Locate every blood parasite and identify its species.
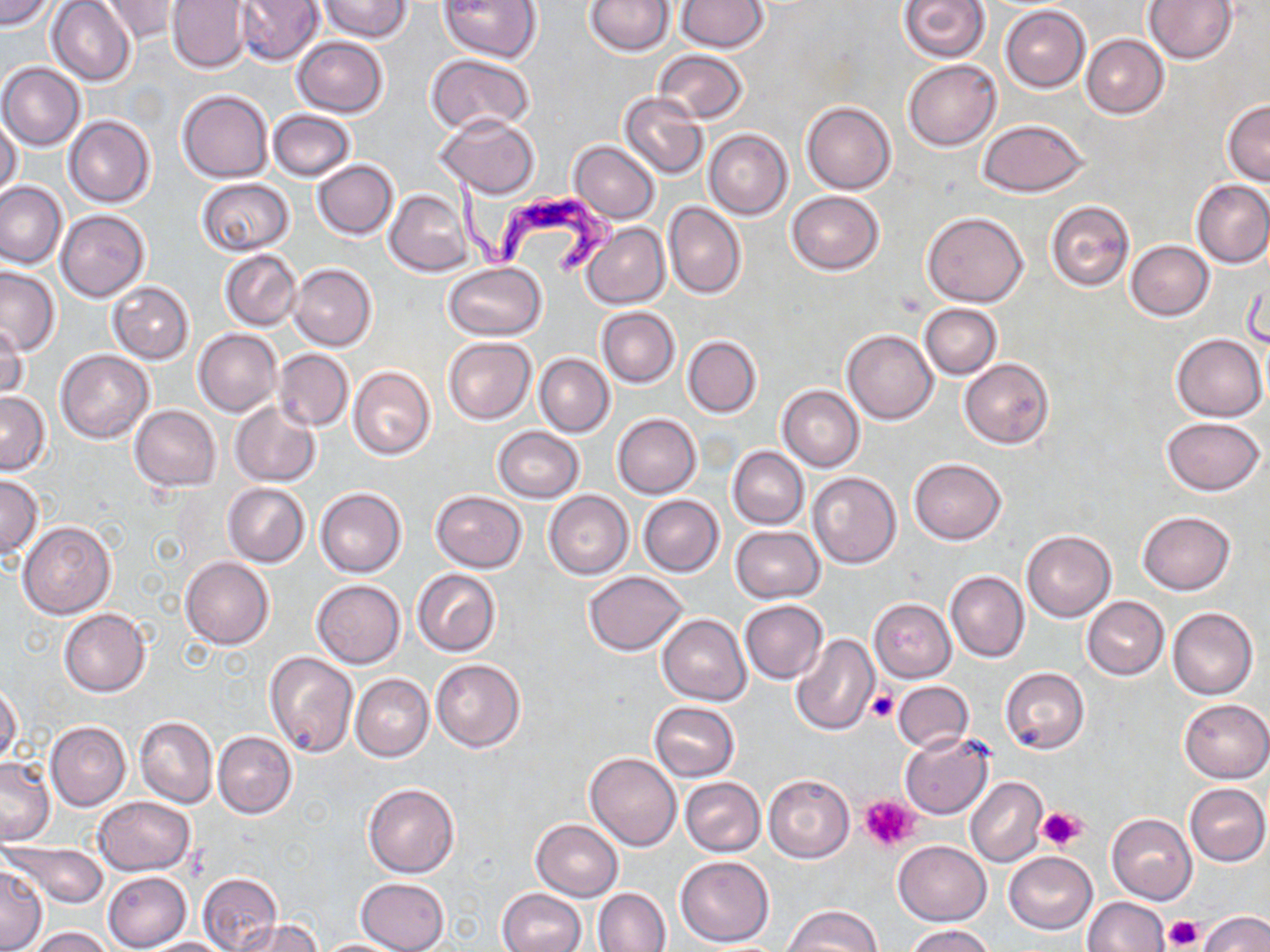
Approximate bounding boxes as [x1, y1, x2, y2] in pixels.
Trypanosoma brucei: [450, 177, 622, 278].
No Plasmodium falciparum, Plasmodium ovale, Plasmodium malariae, Plasmodium vivax, or Babesia divergens observed.

Uninfected red blood cell locations: [0, 0, 54, 31], [100, 0, 181, 43], [167, 0, 252, 73], [233, 0, 324, 66], [317, 0, 412, 41], [437, 0, 543, 63], [676, 0, 768, 52], [897, 0, 990, 62], [1144, 0, 1238, 64], [47, 1, 136, 85], [584, 1, 675, 56], [1001, 5, 1090, 92], [1081, 34, 1169, 119], [291, 36, 388, 117], [652, 50, 749, 124], [427, 54, 536, 135], [903, 59, 1001, 152], [1, 62, 85, 151], [177, 90, 272, 183], [620, 90, 707, 180], [1222, 99, 1270, 185], [802, 101, 897, 194], [268, 109, 357, 180], [433, 113, 539, 198], [0, 115, 23, 199], [63, 115, 154, 208], [977, 118, 1089, 197], [704, 129, 792, 218], [568, 141, 660, 222], [312, 160, 399, 239], [197, 179, 294, 255], [1191, 179, 1270, 268], [0, 181, 66, 269], [385, 189, 472, 277], [785, 190, 885, 275], [1046, 200, 1134, 291], [664, 202, 746, 299], [56, 210, 149, 303], [922, 210, 1029, 307], [582, 223, 670, 309], [1125, 240, 1214, 320], [219, 249, 303, 330], [444, 262, 546, 340], [288, 263, 377, 350], [0, 266, 59, 356], [107, 281, 195, 364], [918, 303, 1003, 379], [597, 307, 679, 387], [1, 323, 27, 399], [194, 329, 282, 417], [842, 330, 938, 424], [1170, 334, 1267, 420], [682, 336, 762, 417], [443, 337, 536, 423], [274, 348, 353, 433], [55, 349, 152, 443], [535, 354, 614, 437], [959, 358, 1054, 448], [347, 367, 435, 460], [777, 385, 864, 471], [0, 392, 51, 474], [229, 401, 321, 486], [130, 405, 220, 491], [612, 413, 701, 499], [1162, 417, 1264, 494], [492, 427, 584, 503], [728, 447, 808, 529], [908, 458, 1006, 545], [807, 471, 900, 568], [0, 474, 42, 559], [222, 483, 310, 567], [314, 487, 407, 577], [545, 490, 633, 579], [431, 491, 527, 572], [638, 495, 724, 577], [1137, 511, 1235, 594], [18, 521, 116, 618], [730, 526, 825, 604], [1022, 530, 1116, 622], [181, 556, 273, 649], [413, 568, 500, 656], [946, 570, 1029, 661], [582, 572, 688, 656], [311, 580, 406, 668], [1081, 596, 1169, 680], [869, 598, 956, 681], [739, 599, 828, 684], [1168, 607, 1257, 699], [58, 608, 150, 697], [657, 614, 751, 705], [790, 634, 878, 736], [264, 650, 357, 757], [431, 659, 526, 753], [1000, 667, 1089, 754], [351, 674, 434, 761], [893, 681, 974, 754], [0, 683, 22, 768], [1180, 699, 1269, 783], [648, 701, 740, 781], [134, 716, 216, 808], [45, 721, 131, 811], [212, 731, 296, 818], [899, 732, 994, 819], [585, 753, 680, 851], [0, 755, 55, 845], [763, 774, 855, 862], [679, 777, 765, 857], [965, 777, 1048, 866], [362, 781, 460, 878], [1185, 783, 1269, 865], [92, 797, 196, 875], [1106, 814, 1198, 905], [530, 819, 623, 902], [893, 840, 991, 925], [4, 841, 108, 909], [1004, 851, 1096, 934], [674, 855, 775, 947], [0, 865, 46, 951], [102, 871, 191, 952], [197, 873, 283, 952], [356, 877, 449, 952], [592, 888, 671, 951], [496, 889, 585, 952], [1082, 897, 1169, 952], [783, 904, 882, 952], [1197, 910, 1270, 952], [233, 918, 322, 952], [903, 925, 996, 952], [26, 926, 116, 952], [139, 937, 233, 951], [313, 938, 408, 951]. Platelet locations: [868, 689, 898, 723], [858, 795, 919, 850], [1037, 807, 1084, 851], [1166, 916, 1202, 949]. Slide-level diagnosis: Trypanosoma brucei. Optical microscopy. Captured at 1000x magnification. Single field of view. May-Grünwald-Giemsa stain. Image is 1270×952 pixels. Thin blood film.